Assess this cell for malaria.
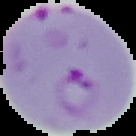
Parasitized.

Summary:
  - Image size: 136×136 pixels
  - Preparation: thin blood film
  - Image type: cell region segmented out of the field of view; surrounding area masked to black